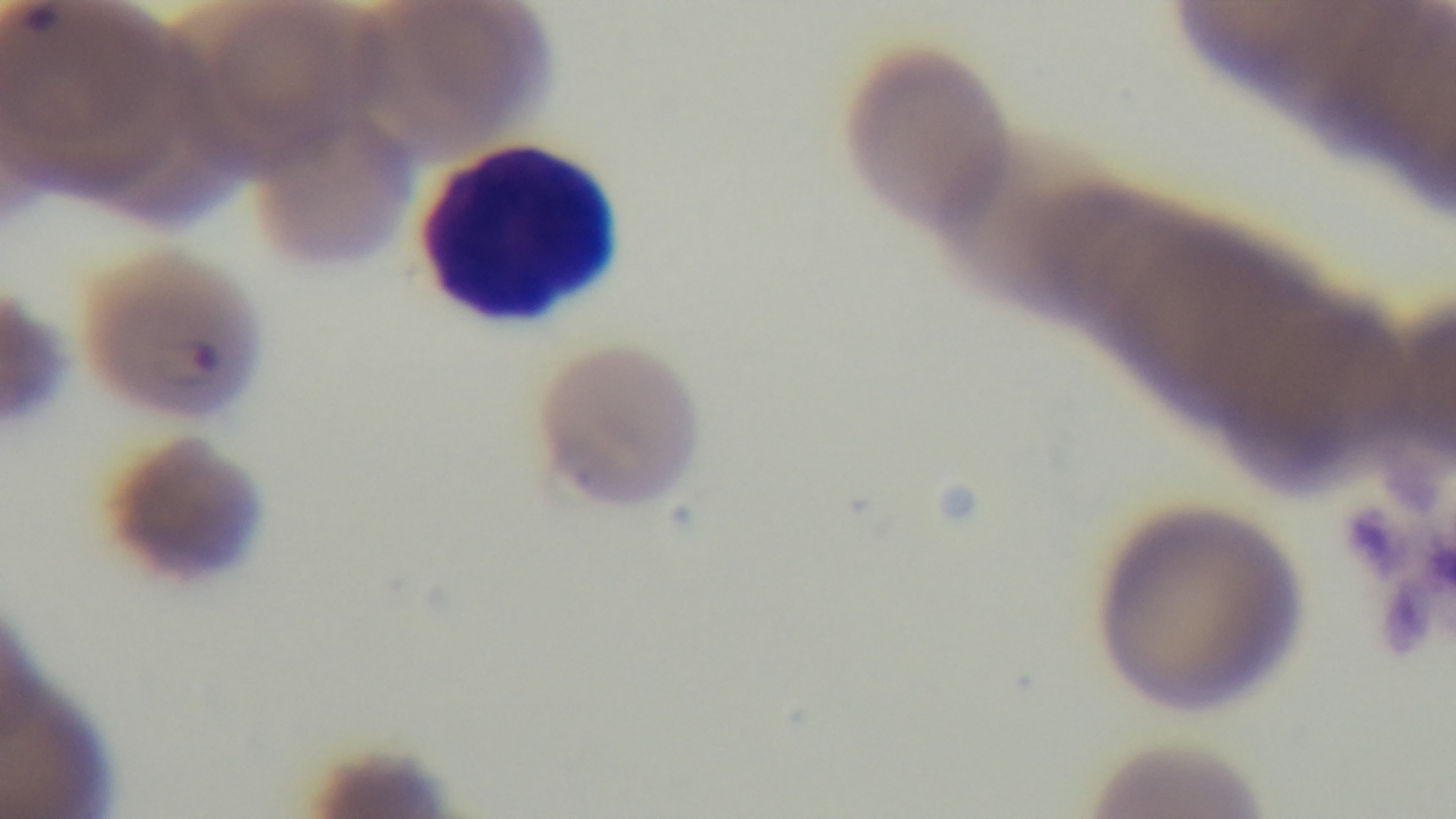 Light microscopy. Mounted 4K digital camera. Preparation: thin smear. Oil-immersion objective, 100x. Giemsa-stained. Malaria status: infected. One field from the slide.